Locate and identify every blood parasite.
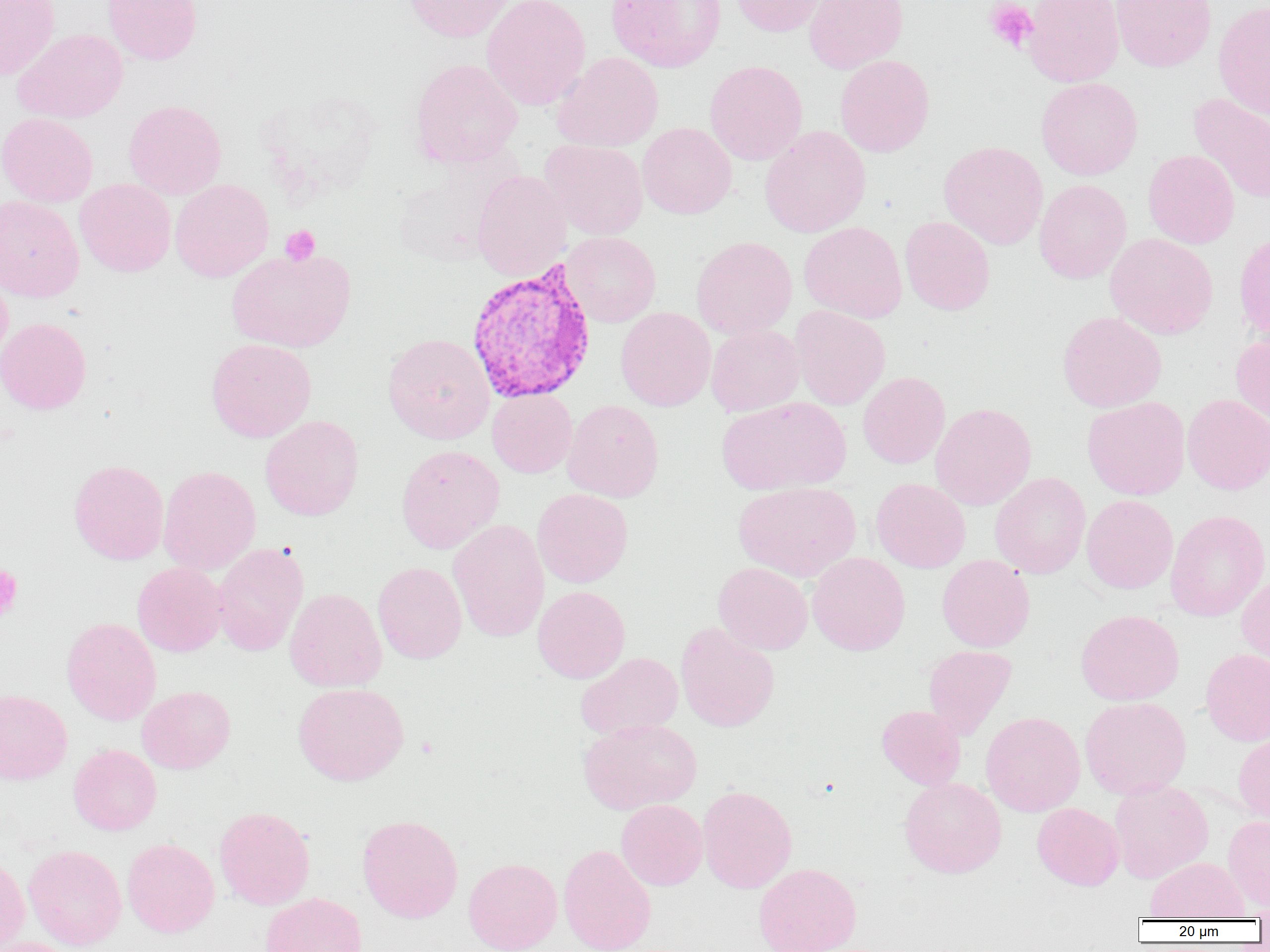
Approximate bounding boxes as (x1, y1, x2, y2) in pixels.
Plasmodium vivax-infected red blood cells: (465, 261, 598, 405).
No Plasmodium falciparum, Plasmodium ovale, Plasmodium malariae, Babesia divergens, or Trypanosoma brucei observed.

slide_level_diagnosis: Plasmodium vivax
image_size: 1270×952 pixels
field_of_view: single
magnification: 1000x
preparation: thin blood film
platelet_locations: 'approximate bounding boxes as (x1, y1, x2, y2) in pixels: (984, 1, 1039, 54), (280, 225, 320, 266), (0, 564, 23, 622)'
modality: light microscopy
uninfected_red_blood_cell_locations: 'approximate bounding boxes as (x1, y1, x2, y2) in pixels: (0, 0, 60, 80), (102, 0, 202, 65), (402, 0, 514, 42), (481, 0, 591, 110), (606, 0, 726, 72), (729, 0, 831, 37), (804, 0, 908, 74), (1023, 0, 1124, 87), (1110, 0, 1216, 72), (1213, 1, 1270, 121), (13, 28, 128, 123), (552, 52, 663, 152), (835, 54, 934, 157), (410, 58, 523, 168), (704, 60, 807, 165), (1036, 77, 1143, 180), (1188, 93, 1270, 205), (123, 99, 226, 199), (0, 112, 98, 207), (637, 122, 736, 219), (760, 125, 871, 237), (540, 140, 648, 239), (938, 141, 1048, 249), (1143, 149, 1240, 249), (391, 157, 515, 268), (471, 170, 571, 281), (74, 178, 176, 276), (170, 179, 274, 282), (1034, 180, 1132, 283), (0, 195, 84, 302), (900, 216, 995, 315), (799, 221, 907, 322), (561, 232, 661, 326), (1105, 233, 1218, 339), (691, 236, 797, 339), (226, 247, 356, 352), (0, 267, 13, 366), (615, 306, 715, 411), (790, 306, 890, 410), (1057, 311, 1167, 412), (0, 317, 91, 414), (706, 325, 805, 416), (382, 333, 495, 444), (1230, 333, 1270, 428), (206, 338, 316, 442), (857, 371, 950, 468), (487, 389, 577, 478), (1182, 393, 1270, 494), (717, 397, 851, 495), (1082, 397, 1190, 500), (562, 399, 664, 502), (930, 402, 1036, 510), (260, 415, 364, 521), (396, 444, 505, 553), (69, 459, 169, 564), (158, 465, 261, 575), (990, 472, 1091, 578), (870, 478, 971, 573), (734, 481, 861, 581), (532, 489, 633, 588), (1081, 494, 1178, 594), (1165, 509, 1269, 621), (448, 519, 549, 642), (212, 542, 309, 656), (807, 552, 910, 656), (936, 555, 1035, 652), (373, 561, 467, 664), (713, 562, 813, 655), (132, 563, 227, 656), (1236, 573, 1270, 673), (533, 585, 630, 683), (284, 588, 387, 692), (1075, 609, 1184, 705), (61, 617, 161, 725), (676, 622, 780, 732), (923, 645, 1016, 739), (1201, 648, 1270, 746), (576, 652, 683, 739), (293, 682, 409, 785), (136, 686, 235, 774), (0, 688, 72, 785), (1080, 696, 1191, 799), (876, 705, 966, 790), (981, 711, 1085, 816), (578, 719, 702, 814), (1233, 731, 1270, 827), (68, 744, 162, 835), (899, 777, 1006, 878), (1108, 780, 1213, 883), (698, 785, 797, 893), (616, 799, 707, 890), (1032, 803, 1124, 890), (214, 806, 315, 910), (357, 814, 463, 923), (1222, 816, 1270, 913), (122, 838, 219, 938), (23, 844, 127, 950), (558, 844, 657, 952), (0, 853, 30, 952), (1146, 857, 1248, 920), (463, 858, 562, 952), (753, 862, 861, 952), (260, 892, 366, 952), (1, 937, 82, 952)'